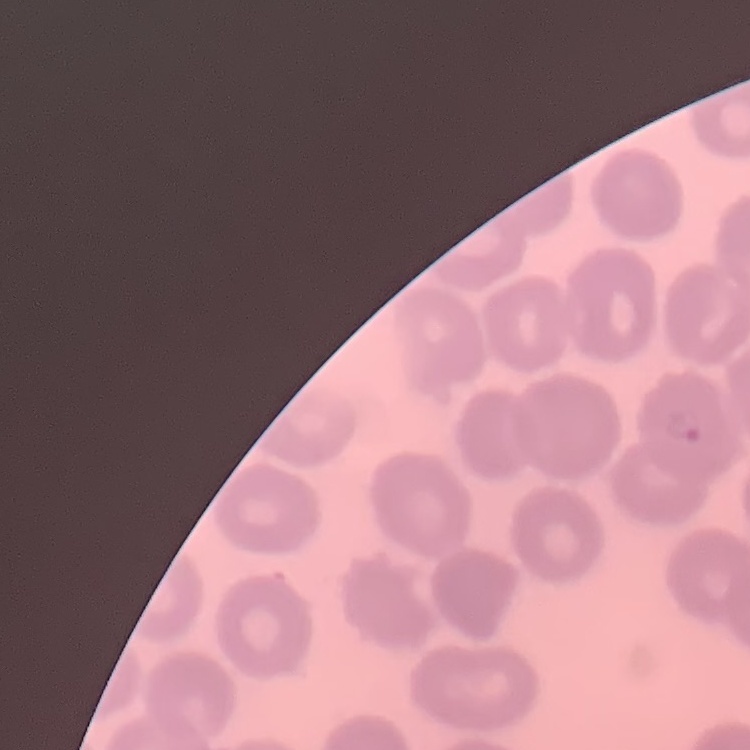

red blood cell morphology = no rouleaux formation
image type = square crop of a larger photomicrograph
stain = Field's or Giemsa
preparation = thin peripheral smear